Describe the morphology of the red blood cells.
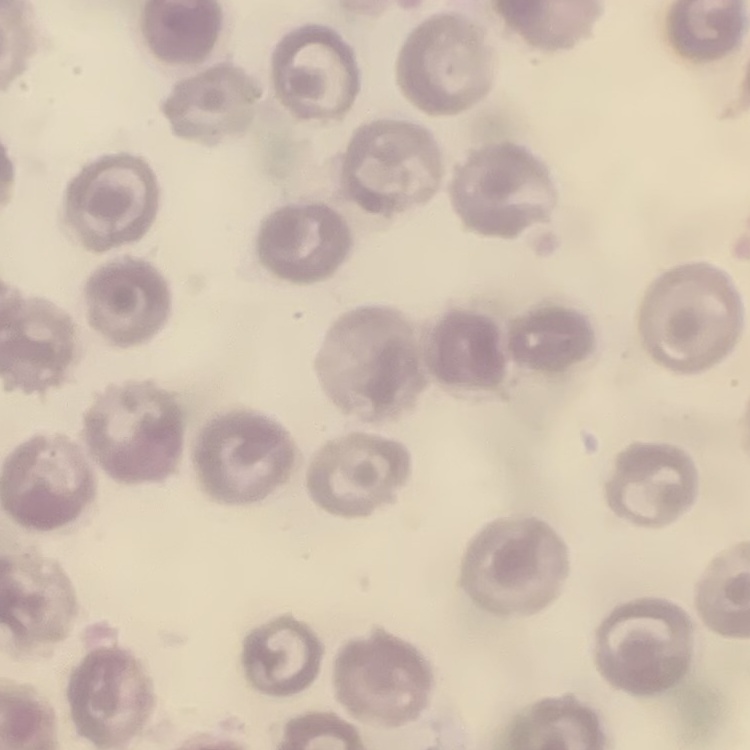
They show no rouleaux formation.

image type = one tile cut from a larger photomicrograph
stain = Field's or Giemsa
preparation = thin peripheral smear